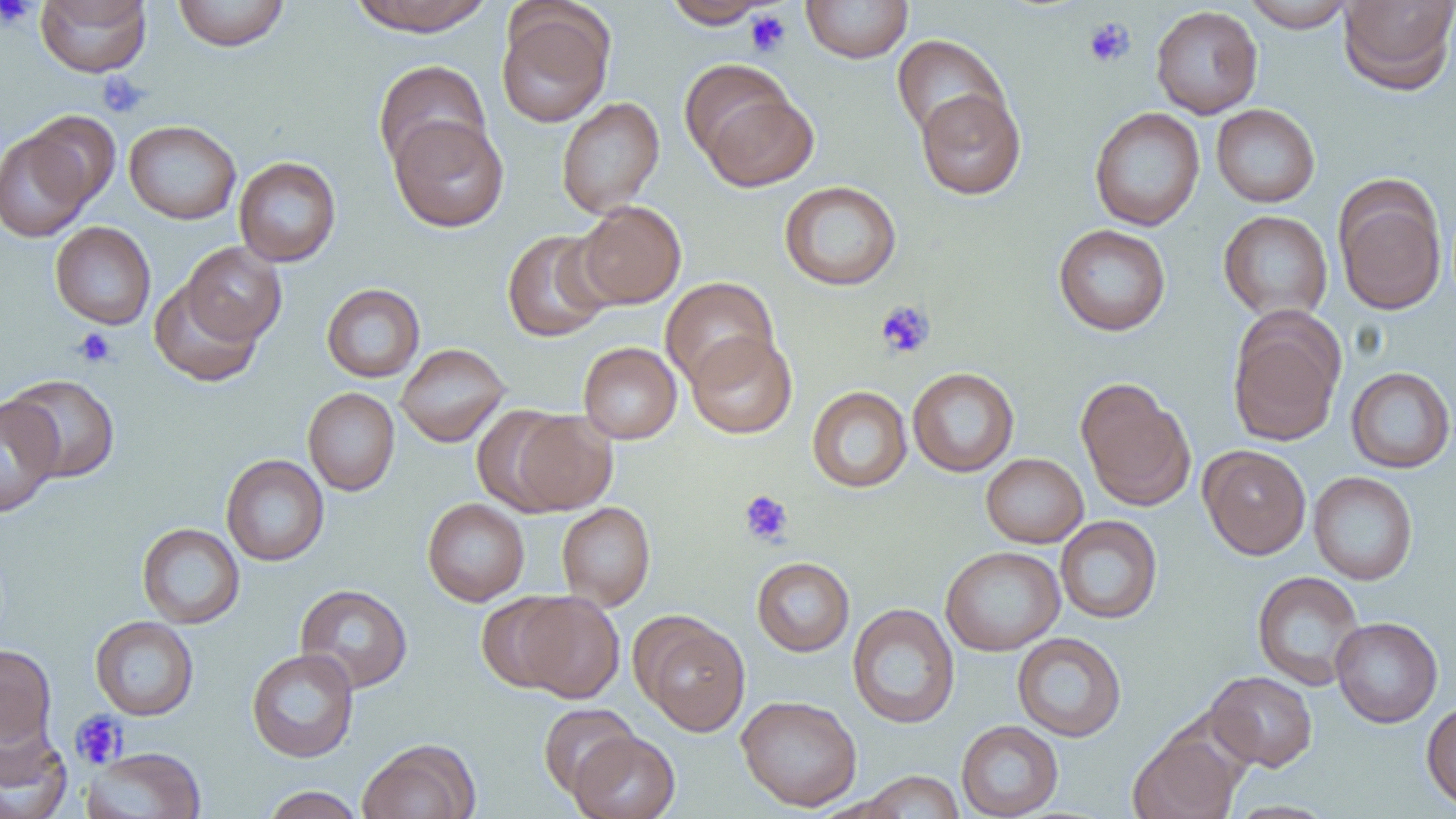 Approximate bounding boxes as [x1, y1, x2, y2] in pixels. Uninfected red blood cell locations: [36, 0, 152, 77], [172, 0, 290, 51], [347, 0, 494, 36], [801, 0, 913, 63], [1242, 0, 1356, 32], [1338, 0, 1456, 94], [662, 1, 775, 28], [496, 5, 614, 128], [1150, 5, 1263, 119], [891, 35, 1009, 143], [373, 59, 491, 173], [697, 84, 819, 191], [915, 87, 1026, 200], [556, 96, 665, 218], [1211, 104, 1320, 207], [1089, 107, 1205, 231], [23, 111, 121, 208], [389, 115, 509, 232], [124, 120, 241, 224], [0, 130, 95, 242], [234, 157, 341, 267], [1334, 177, 1447, 316], [779, 181, 902, 291], [575, 201, 686, 309], [1218, 210, 1333, 322], [50, 221, 156, 329], [1053, 224, 1171, 336], [501, 228, 615, 342], [180, 242, 287, 345], [660, 276, 779, 388], [149, 280, 263, 387], [321, 283, 426, 382], [1228, 313, 1345, 446], [686, 332, 797, 439], [578, 341, 682, 444], [396, 343, 510, 447], [1345, 366, 1456, 473], [907, 367, 1019, 477], [4, 374, 120, 482], [1075, 378, 1196, 511], [807, 386, 912, 493], [303, 387, 400, 496], [0, 396, 63, 518], [505, 409, 617, 516], [1199, 445, 1312, 559], [981, 453, 1088, 548], [221, 454, 329, 566], [1308, 471, 1418, 585], [422, 498, 530, 606], [556, 502, 655, 611], [1055, 516, 1163, 624], [137, 523, 245, 628], [940, 546, 1065, 656], [751, 557, 855, 657], [1251, 570, 1366, 690], [294, 584, 413, 694], [476, 592, 577, 694], [514, 593, 624, 703], [846, 603, 960, 729], [90, 616, 199, 721], [636, 616, 750, 736], [1331, 616, 1443, 727], [1012, 632, 1127, 742], [0, 644, 57, 748], [246, 648, 359, 762], [1205, 670, 1318, 771], [736, 695, 862, 811], [1421, 699, 1456, 812], [538, 703, 639, 798], [956, 720, 1064, 818], [0, 724, 72, 819], [1129, 729, 1244, 819], [569, 730, 681, 819], [358, 739, 480, 819], [80, 746, 207, 819], [859, 770, 964, 818], [260, 785, 364, 819], [1223, 800, 1341, 819]. Platelet locations: [0, 0, 37, 30], [745, 10, 791, 57], [1083, 17, 1136, 68], [96, 72, 149, 119], [874, 299, 935, 360], [73, 327, 116, 368], [740, 490, 794, 546], [70, 710, 128, 769]. Slide-level diagnosis: negative for blood parasites. 1000x magnification. Single field of view. Thin blood smear. Image is 1456×819 pixels. Optical microscopy.